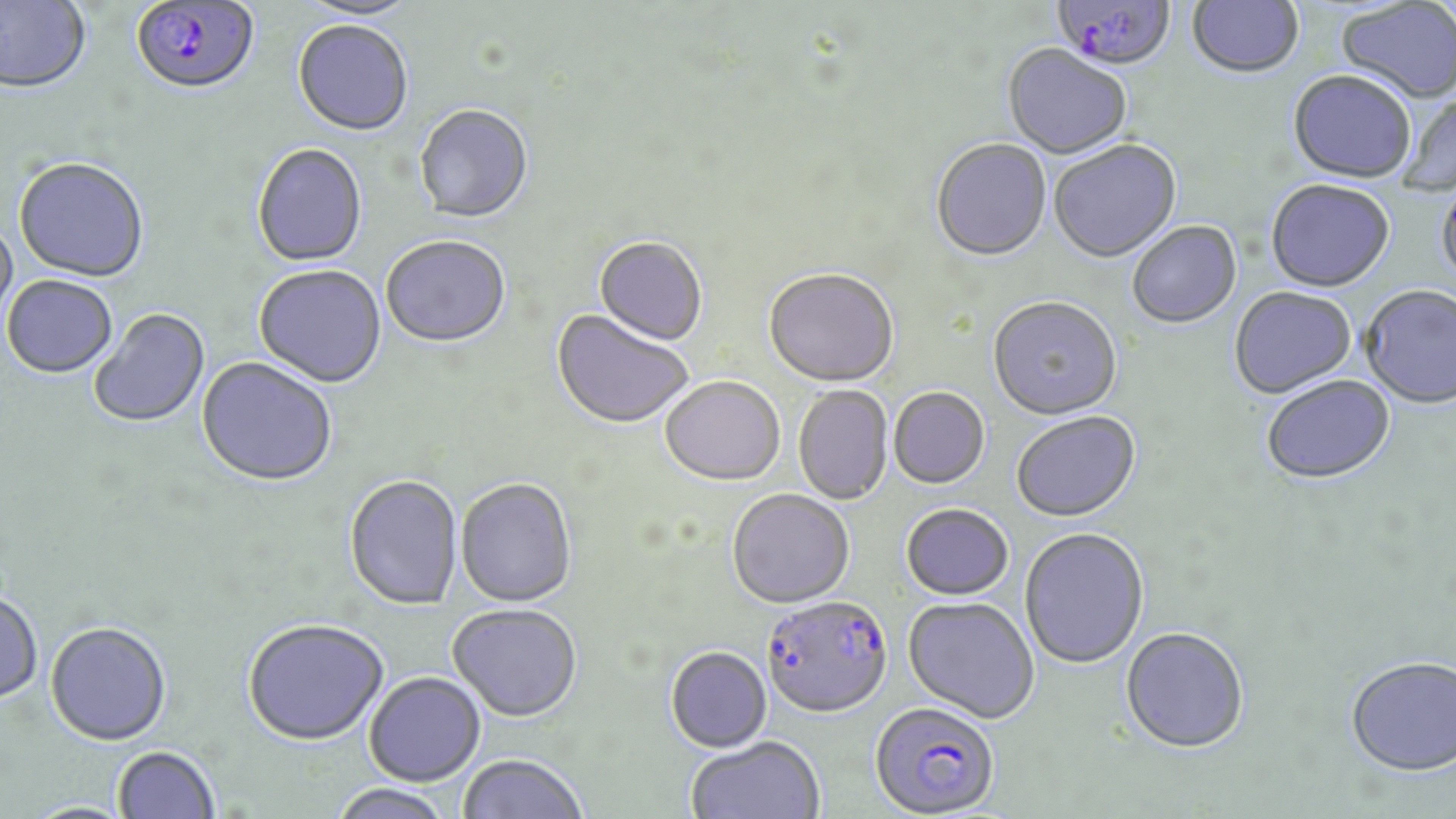

Summary:
  - Coordinate format: approximate bounding boxes as [x1, y1, x2, y2] in pixels
  - Plasmodium falciparum-infected red blood cell locations: [1050, 0, 1176, 74], [131, 2, 260, 99], [762, 598, 893, 721], [869, 704, 999, 818]
  - Uninfected red blood cell locations: [1187, 0, 1304, 82], [0, 1, 92, 95], [296, 1, 422, 24], [1336, 1, 1456, 105], [293, 22, 413, 138], [1001, 46, 1131, 160], [1287, 72, 1417, 186], [1398, 90, 1456, 196], [414, 107, 534, 225], [931, 140, 1052, 264], [1048, 141, 1183, 265], [252, 144, 367, 268], [13, 159, 149, 284], [1265, 182, 1394, 294], [1436, 184, 1456, 290], [0, 217, 18, 333], [1127, 222, 1242, 330], [594, 238, 707, 347], [381, 239, 510, 350], [254, 266, 387, 390], [763, 271, 899, 390], [2, 277, 117, 381], [1229, 288, 1357, 400], [1361, 288, 1456, 411], [988, 299, 1122, 422], [89, 308, 210, 429], [551, 311, 693, 431], [196, 358, 337, 489], [1261, 378, 1396, 488], [660, 379, 785, 488], [793, 386, 893, 506], [888, 389, 990, 490], [1011, 413, 1141, 525], [344, 476, 463, 611], [455, 479, 577, 608], [728, 491, 855, 610], [901, 506, 1013, 602], [1019, 529, 1149, 670], [0, 590, 43, 704], [902, 598, 1039, 724], [447, 603, 583, 723], [243, 618, 389, 745], [45, 622, 171, 746], [1120, 629, 1250, 756], [665, 647, 771, 752], [1346, 656, 1456, 778], [364, 671, 485, 786], [686, 737, 825, 819], [114, 745, 220, 819], [457, 754, 587, 818], [329, 783, 457, 819], [23, 800, 137, 819]
  - Slide-level diagnosis: Plasmodium falciparum
  - Magnification: 1000x
  - Modality: optical microscopy
  - Field of view: one of a larger specimen
  - Stain: May-Grünwald-Giemsa
  - Preparation: thin blood film
  - Image size: 1456×819 pixels